Give the extent of all uninfected red blood cells.
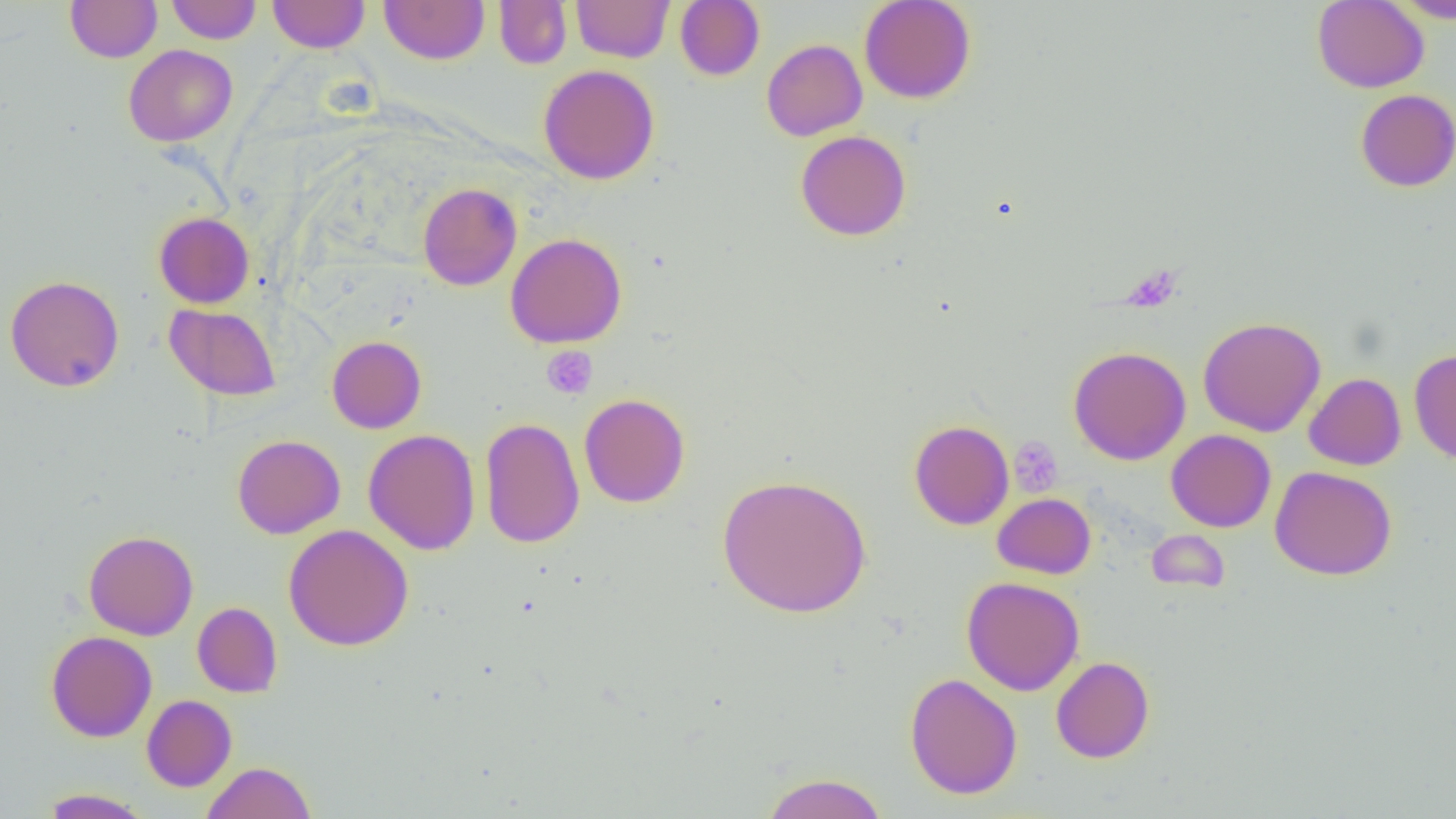
Approximate bounding boxes as named x1/y1/x2/y2 corners in pixels.
Uninfected red blood cells: (x1=65, y1=0, x2=162, y2=63), (x1=166, y1=0, x2=261, y2=44), (x1=267, y1=0, x2=370, y2=53), (x1=379, y1=0, x2=490, y2=65), (x1=571, y1=0, x2=674, y2=62), (x1=675, y1=0, x2=765, y2=81), (x1=859, y1=0, x2=976, y2=104), (x1=1312, y1=0, x2=1429, y2=93), (x1=1390, y1=0, x2=1456, y2=23), (x1=494, y1=1, x2=572, y2=69), (x1=761, y1=39, x2=867, y2=141), (x1=123, y1=44, x2=237, y2=146), (x1=538, y1=64, x2=660, y2=185), (x1=1355, y1=89, x2=1456, y2=192), (x1=795, y1=130, x2=911, y2=241), (x1=417, y1=183, x2=522, y2=291), (x1=154, y1=212, x2=254, y2=308), (x1=505, y1=232, x2=627, y2=348), (x1=5, y1=274, x2=124, y2=392), (x1=164, y1=303, x2=281, y2=401), (x1=1198, y1=316, x2=1326, y2=436), (x1=327, y1=335, x2=426, y2=433), (x1=1068, y1=346, x2=1191, y2=465), (x1=1409, y1=348, x2=1456, y2=464), (x1=1304, y1=373, x2=1406, y2=470), (x1=579, y1=393, x2=690, y2=508), (x1=479, y1=417, x2=585, y2=548), (x1=909, y1=420, x2=1014, y2=530), (x1=363, y1=429, x2=481, y2=555), (x1=1166, y1=430, x2=1276, y2=532), (x1=232, y1=435, x2=344, y2=538), (x1=1270, y1=465, x2=1397, y2=580), (x1=716, y1=473, x2=872, y2=619), (x1=993, y1=493, x2=1096, y2=579), (x1=283, y1=523, x2=414, y2=651), (x1=1146, y1=528, x2=1229, y2=594), (x1=83, y1=530, x2=198, y2=640), (x1=960, y1=576, x2=1085, y2=696), (x1=192, y1=602, x2=282, y2=697), (x1=45, y1=630, x2=157, y2=742), (x1=1050, y1=656, x2=1155, y2=763), (x1=905, y1=673, x2=1022, y2=799), (x1=142, y1=695, x2=237, y2=791), (x1=201, y1=761, x2=317, y2=819), (x1=761, y1=772, x2=889, y2=819), (x1=39, y1=788, x2=152, y2=818).

Platelet locations: (x1=541, y1=347, x2=597, y2=399), (x1=1008, y1=437, x2=1063, y2=495). Slide-level diagnosis: negative for blood parasites. Thin blood smear. Optical microscopy. Single field of view. 1000x magnification. Image is 1456×819 pixels.